Identify the blood parasite species.
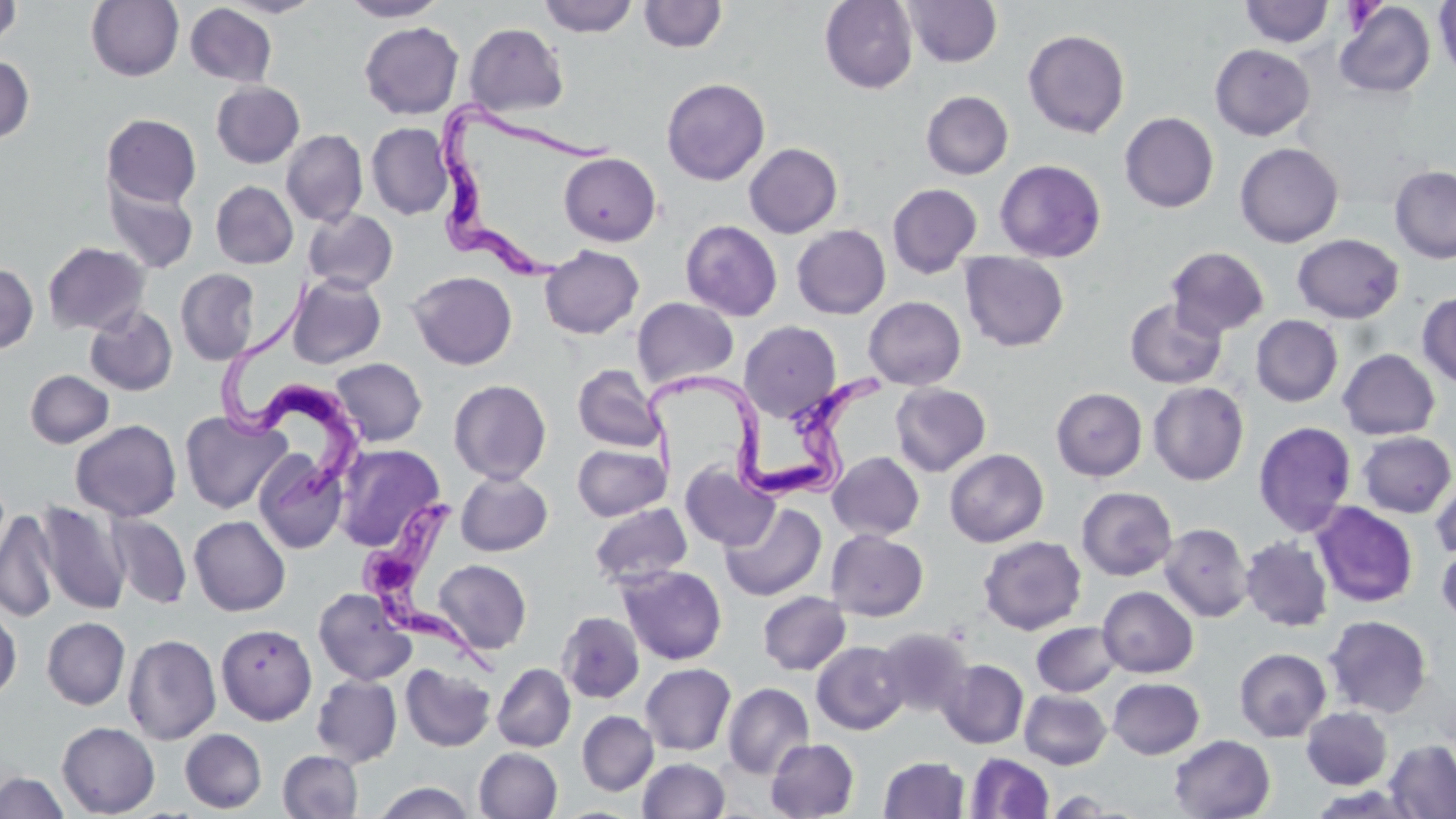

Trypanosoma brucei.

Summary:
  - Coordinate format: approximate bounding boxes as (x1, y1, x2, y2) in pixels
  - Uninfected red blood cell locations: (220, 0, 324, 18), (339, 0, 448, 21), (539, 0, 638, 37), (819, 0, 918, 93), (902, 0, 1002, 68), (1434, 0, 1456, 80), (0, 1, 21, 48), (86, 1, 183, 81), (638, 1, 727, 53), (1239, 1, 1334, 47), (1334, 2, 1435, 98), (185, 3, 277, 87), (359, 22, 463, 119), (464, 23, 568, 117), (1023, 29, 1130, 138), (1210, 44, 1315, 140), (0, 54, 35, 145), (661, 78, 770, 185), (211, 81, 305, 168), (921, 91, 1013, 179), (1120, 112, 1219, 213), (101, 113, 202, 209), (366, 122, 453, 220), (281, 129, 368, 227), (1234, 142, 1344, 248), (744, 143, 843, 238), (559, 152, 661, 246), (994, 159, 1106, 262), (1389, 164, 1456, 264), (104, 177, 199, 274), (210, 181, 298, 269), (887, 183, 982, 278), (303, 209, 398, 294), (680, 219, 783, 321), (792, 225, 890, 319), (1292, 234, 1405, 324), (42, 242, 150, 335), (540, 245, 644, 339), (1166, 246, 1270, 338), (960, 252, 1069, 352), (0, 262, 38, 354), (175, 268, 260, 366), (408, 271, 517, 370), (287, 274, 386, 369), (1417, 291, 1456, 388), (863, 296, 966, 390), (632, 297, 740, 389), (1125, 298, 1227, 389), (84, 305, 178, 396), (1250, 315, 1343, 407), (739, 321, 841, 422), (1337, 349, 1440, 440), (330, 358, 427, 447), (573, 364, 666, 452), (25, 370, 114, 449), (448, 379, 551, 484), (1148, 381, 1249, 485), (891, 383, 991, 476), (1050, 387, 1148, 481), (180, 410, 290, 514), (70, 419, 181, 521), (1253, 421, 1357, 536), (1357, 431, 1455, 518), (333, 443, 446, 552), (572, 443, 670, 521), (944, 448, 1049, 548), (253, 451, 348, 554), (828, 451, 924, 540), (680, 462, 779, 552), (455, 471, 553, 556), (1431, 471, 1456, 564), (1076, 487, 1177, 581), (36, 500, 130, 615), (590, 502, 692, 588), (720, 502, 827, 601), (1311, 502, 1419, 608), (0, 508, 60, 623), (107, 513, 192, 609), (189, 516, 291, 616), (1159, 523, 1253, 622), (826, 530, 928, 621), (978, 535, 1087, 635), (1240, 536, 1333, 632), (1437, 542, 1456, 628), (433, 559, 532, 654), (617, 564, 727, 665), (1097, 586, 1198, 678), (313, 587, 416, 686), (757, 591, 851, 675), (0, 605, 21, 701), (557, 611, 645, 704), (1324, 614, 1432, 718), (42, 617, 130, 710), (1031, 621, 1122, 696), (216, 624, 317, 724), (875, 627, 973, 718), (123, 634, 221, 744), (812, 641, 910, 734), (1234, 648, 1331, 742), (937, 659, 1029, 749), (400, 663, 496, 751), (492, 663, 575, 751), (640, 663, 736, 756), (312, 675, 402, 767), (1107, 677, 1205, 759), (722, 682, 814, 779), (1019, 689, 1111, 769), (1301, 707, 1392, 789), (577, 710, 658, 795), (57, 721, 160, 817), (180, 728, 267, 813), (1169, 734, 1275, 819), (765, 738, 859, 818), (1384, 739, 1456, 819), (474, 747, 563, 819), (278, 750, 363, 818), (965, 751, 1054, 818), (878, 756, 970, 818), (638, 758, 730, 818), (0, 772, 68, 818), (372, 781, 476, 819), (1043, 790, 1126, 817)
  - Trypanosoma brucei locations: (438, 90, 617, 286), (213, 275, 370, 510), (646, 365, 881, 505), (357, 493, 507, 684)
  - Magnification: 1000x
  - Preparation: thin blood film
  - Field of view: single
  - Image size: 1456×819 pixels
  - Stain: May-Grünwald-Giemsa
  - Modality: light microscopy